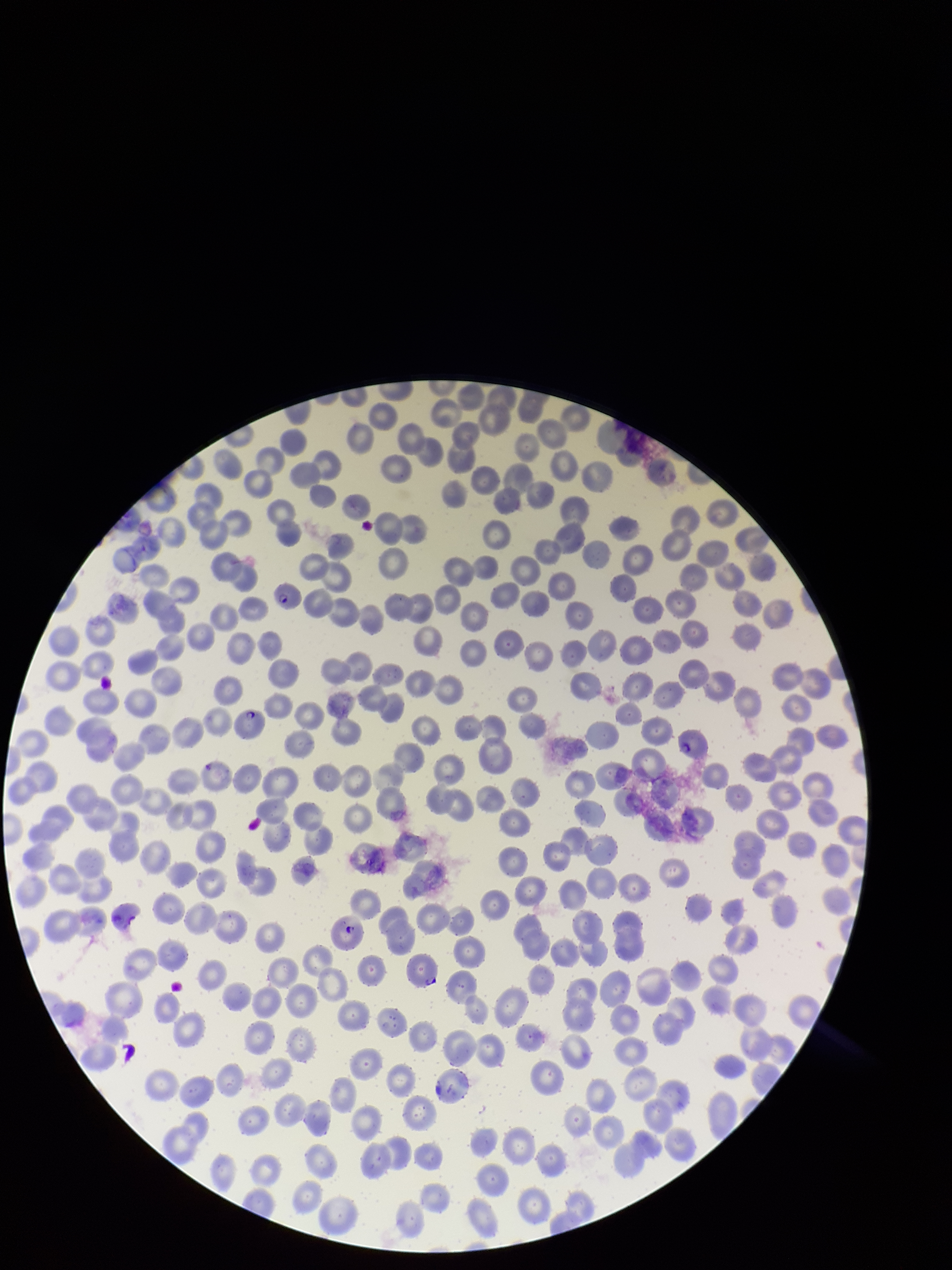
parasitized red blood cell count = 3
stain = Giemsa
patient malaria status = infected
image size = 952×1270 pixels
field of view = single
red blood cell count = 298
preparation = thin smear
parasitized red blood cells = identified
species reported for this patient = Plasmodium falciparum
capture = smartphone photograph through the microscope eyepiece